Assess this cell for malaria.
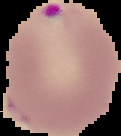
Parasitized.

Summary:
  - Image size: 121×136 pixels
  - Preparation: thin blood smear
  - Image type: segmented cell region on a black background